Assess this cell for malaria.
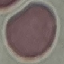
Uninfected.

Summary:
  - Stain: Giemsa
  - Image type: automatically extracted cell patch, resized to 64 × 64 pixels
  - Capture: smartphone camera at the microscope eyepiece
  - Preparation: thin blood film